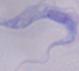
Summary:
  - Magnification: 1000x
  - Modality: micrograph
  - Identification: trypanosome